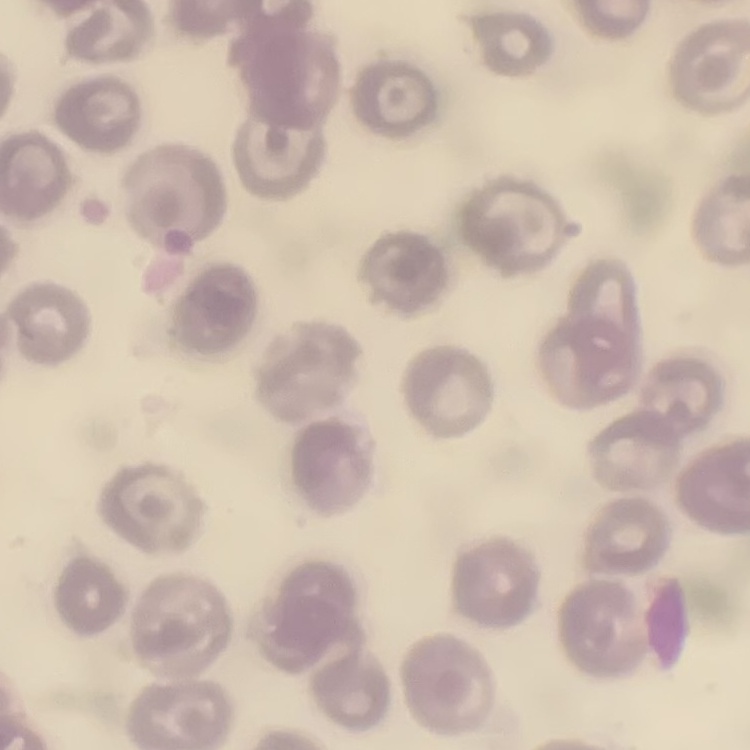
erythrocyte morphology = no rouleaux formation
stain = Field's or Giemsa
image type = one tile cut from a larger photomicrograph
preparation = thin blood film